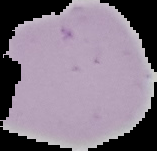
Summary:
  - Malaria status: uninfected
  - Preparation: thin blood film
  - Image size: 157×151 pixels
  - Image type: segmented cell region on a black background